Classify this cell by malaria status.
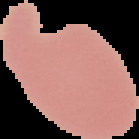
It is uninfected.

From a thin blood smear. Cell region segmented out of the field of view; the surrounding area is masked to black. Image is 139×139 pixels.